Assess this cell for malaria.
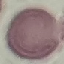
It is uninfected.

{
  "preparation": "thin blood film",
  "image_type": "automatically extracted cell patch, resized to 64 × 64 pixels",
  "stain": "Giemsa",
  "capture": "smartphone through the microscope eyepiece"
}